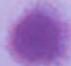

Micrograph. A red blood cell is seen. Captured at 1000x magnification.